Assess the morphology of the erythrocytes.
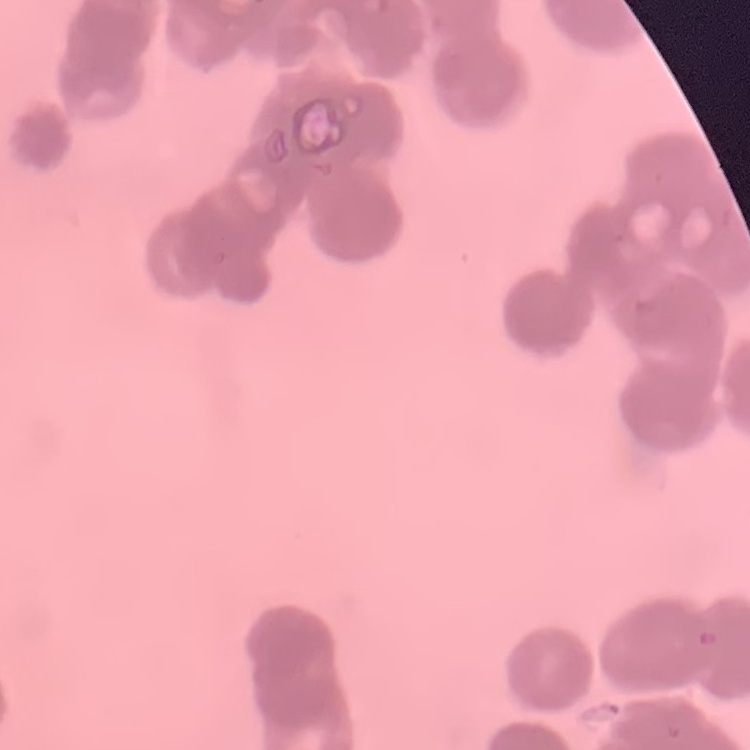
Rouleaux formation.

Stained with either Field's or Giemsa. Thin blood smear. Square crop of a larger photomicrograph.